Give the extent of all Plasmodium falciparum-infected red blood cells.
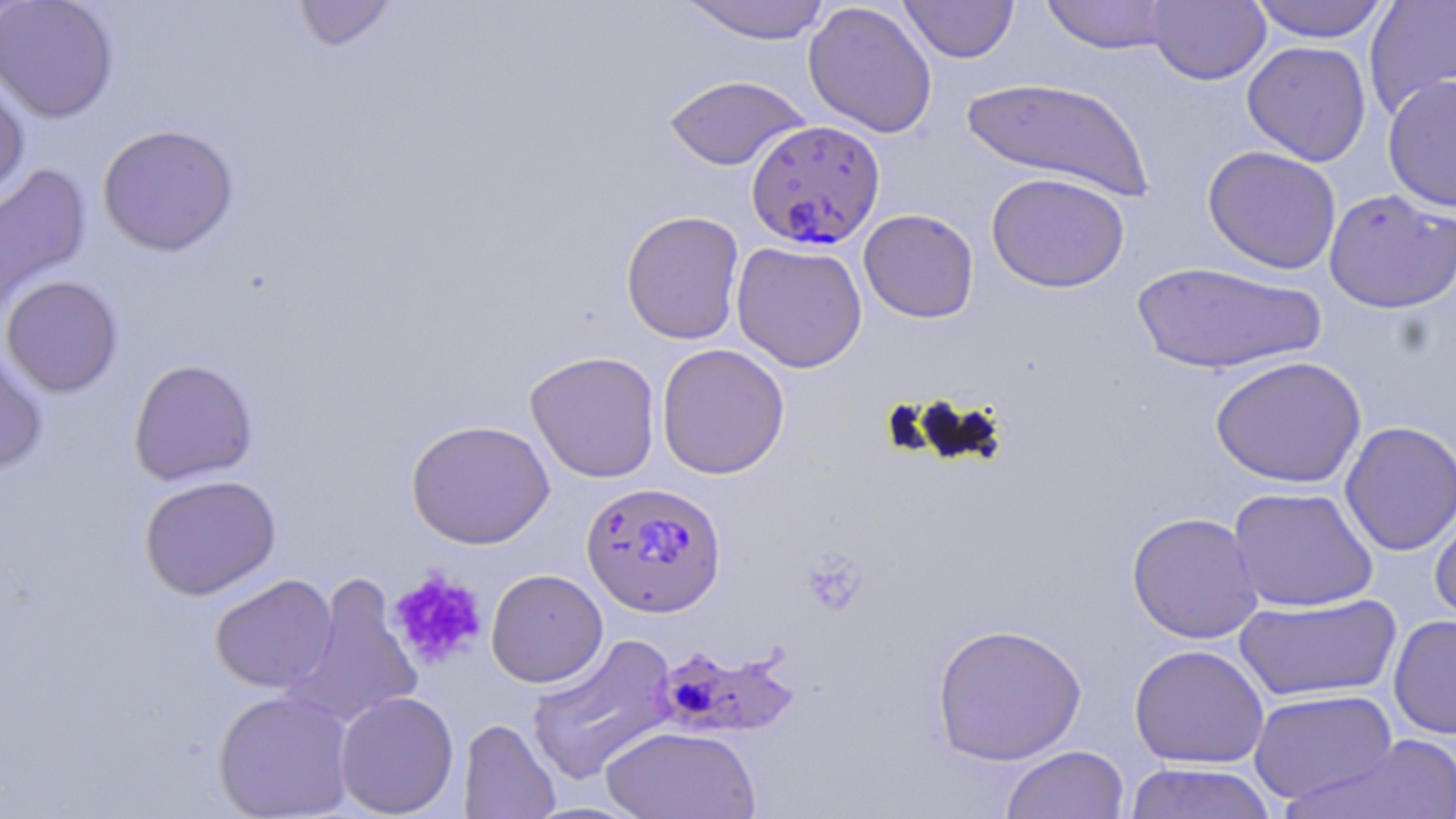
Approximate bounding boxes as (x1, y1, x2, y2) in pixels.
Plasmodium falciparum-infected red blood cells: (745, 119, 885, 250), (581, 481, 727, 617), (650, 640, 799, 740).

Uninfected red blood cell locations: (0, 0, 35, 30), (0, 0, 119, 123), (677, 0, 832, 44), (1040, 0, 1176, 55), (1146, 0, 1271, 85), (1246, 0, 1391, 43), (1364, 0, 1456, 119), (290, 1, 400, 53), (803, 1, 938, 139), (899, 1, 1019, 63), (1242, 40, 1371, 166), (0, 69, 30, 206), (663, 74, 810, 171), (1383, 74, 1456, 212), (961, 76, 1154, 201), (97, 123, 240, 257), (1202, 145, 1342, 275), (0, 162, 92, 316), (986, 172, 1130, 293), (1323, 189, 1456, 314), (858, 209, 979, 323), (621, 210, 745, 345), (731, 241, 868, 373), (1131, 261, 1327, 375), (0, 275, 124, 398), (0, 342, 49, 475), (656, 343, 790, 480), (524, 350, 662, 483), (1210, 355, 1366, 488), (128, 358, 259, 486), (406, 418, 555, 549), (1339, 420, 1456, 556), (139, 474, 281, 600), (1227, 485, 1379, 612), (1430, 504, 1456, 628), (1126, 511, 1264, 644), (486, 569, 608, 688), (210, 574, 337, 693), (283, 575, 423, 730), (1233, 594, 1401, 703), (1388, 614, 1456, 739), (931, 622, 1087, 765), (525, 633, 679, 785), (1129, 644, 1269, 768), (1249, 688, 1397, 805), (212, 689, 355, 819), (334, 690, 459, 818), (458, 719, 560, 818), (601, 725, 761, 819), (1288, 735, 1456, 817), (1000, 744, 1130, 819), (1124, 762, 1277, 819). Platelet locations: (801, 550, 867, 614), (387, 569, 488, 669). Slide-level diagnosis: Plasmodium falciparum. Image is 1456×819 pixels. May-Grünwald-Giemsa stain. Thin blood film. Single field of view. 1000x magnification. Light microscopy.